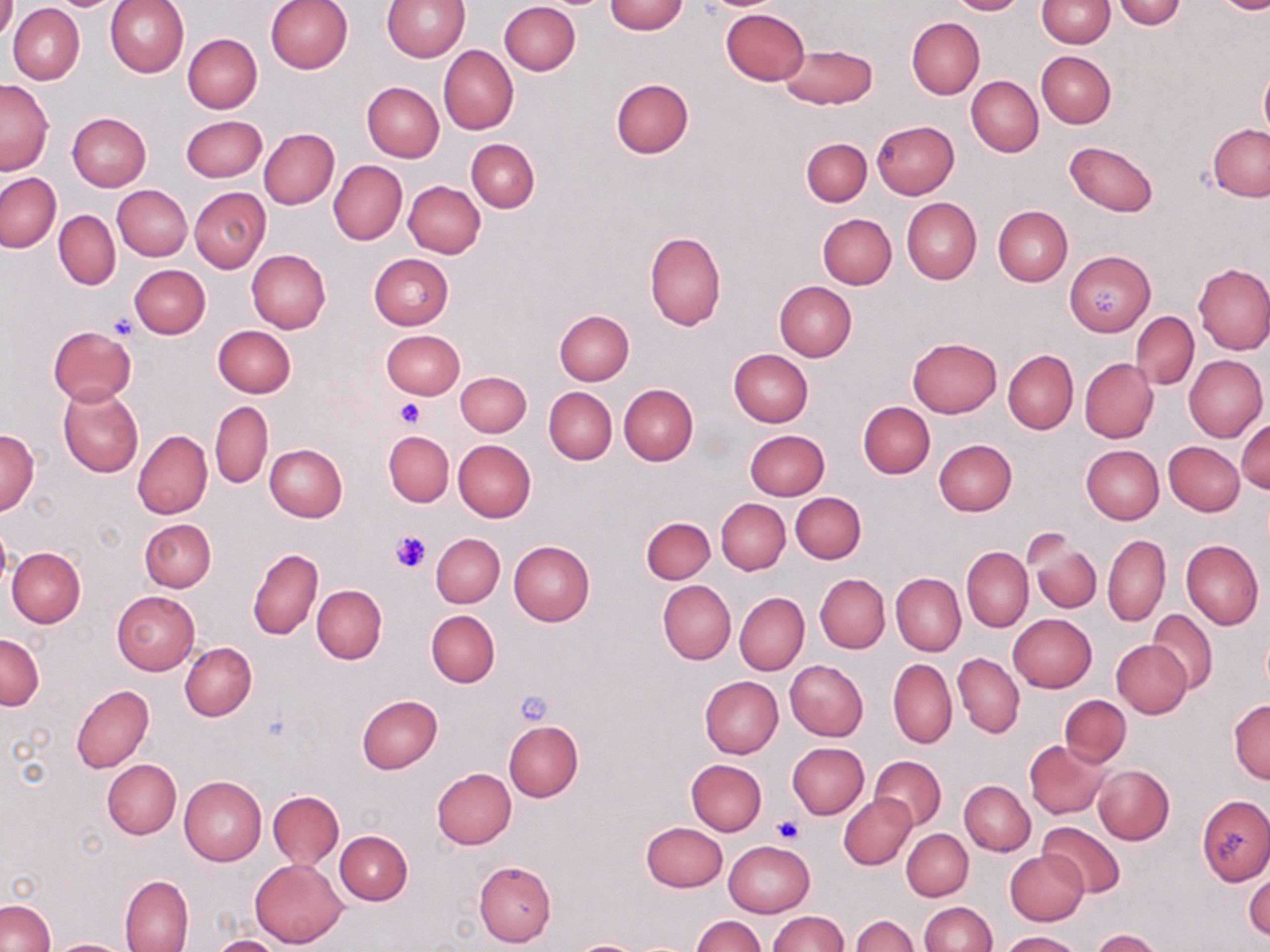

Summary:
  - Coordinate format: approximate bounding boxes as named x1/y1/x2/y2 corners in pixels
  - Platelet locations: (x1=1086, y1=284, x2=1126, y2=320), (x1=108, y1=314, x2=141, y2=340), (x1=395, y1=400, x2=425, y2=427), (x1=389, y1=530, x2=432, y2=574), (x1=514, y1=689, x2=555, y2=728), (x1=774, y1=815, x2=805, y2=843)
  - Uninfected red blood cell locations: (x1=0, y1=0, x2=16, y2=42), (x1=106, y1=0, x2=188, y2=77), (x1=264, y1=0, x2=353, y2=74), (x1=384, y1=0, x2=469, y2=61), (x1=947, y1=0, x2=1028, y2=16), (x1=1037, y1=0, x2=1114, y2=47), (x1=605, y1=1, x2=689, y2=35), (x1=1113, y1=1, x2=1188, y2=27), (x1=1213, y1=1, x2=1270, y2=14), (x1=500, y1=2, x2=581, y2=75), (x1=8, y1=4, x2=84, y2=85), (x1=721, y1=8, x2=808, y2=84), (x1=907, y1=18, x2=985, y2=99), (x1=183, y1=34, x2=261, y2=113), (x1=779, y1=42, x2=876, y2=108), (x1=439, y1=46, x2=518, y2=134), (x1=1036, y1=51, x2=1115, y2=127), (x1=1259, y1=67, x2=1270, y2=141), (x1=967, y1=76, x2=1043, y2=156), (x1=0, y1=79, x2=53, y2=174), (x1=610, y1=79, x2=693, y2=158), (x1=361, y1=82, x2=444, y2=162), (x1=67, y1=113, x2=150, y2=191), (x1=181, y1=115, x2=267, y2=182), (x1=872, y1=121, x2=959, y2=198), (x1=1208, y1=125, x2=1270, y2=200), (x1=259, y1=129, x2=338, y2=210), (x1=801, y1=137, x2=872, y2=207), (x1=466, y1=139, x2=539, y2=213), (x1=1065, y1=142, x2=1158, y2=217), (x1=329, y1=161, x2=407, y2=245), (x1=1, y1=173, x2=61, y2=252), (x1=404, y1=181, x2=485, y2=258), (x1=112, y1=185, x2=192, y2=261), (x1=189, y1=187, x2=270, y2=272), (x1=901, y1=198, x2=980, y2=283), (x1=993, y1=206, x2=1072, y2=286), (x1=53, y1=211, x2=120, y2=290), (x1=817, y1=213, x2=896, y2=289), (x1=645, y1=232, x2=726, y2=330), (x1=247, y1=249, x2=330, y2=333), (x1=1065, y1=250, x2=1155, y2=336), (x1=370, y1=253, x2=453, y2=330), (x1=1193, y1=263, x2=1270, y2=354), (x1=129, y1=264, x2=210, y2=339), (x1=773, y1=281, x2=856, y2=362), (x1=554, y1=310, x2=634, y2=384), (x1=1131, y1=312, x2=1198, y2=390), (x1=213, y1=325, x2=295, y2=397), (x1=48, y1=326, x2=136, y2=405), (x1=381, y1=329, x2=465, y2=399), (x1=908, y1=338, x2=1002, y2=417), (x1=729, y1=348, x2=814, y2=426), (x1=1004, y1=349, x2=1078, y2=434), (x1=739, y1=350, x2=819, y2=498), (x1=1184, y1=354, x2=1267, y2=442), (x1=1080, y1=359, x2=1157, y2=442), (x1=456, y1=371, x2=531, y2=437), (x1=619, y1=383, x2=698, y2=465), (x1=544, y1=386, x2=617, y2=464), (x1=58, y1=387, x2=143, y2=478), (x1=210, y1=401, x2=273, y2=487), (x1=859, y1=402, x2=934, y2=477), (x1=1236, y1=418, x2=1269, y2=493), (x1=0, y1=430, x2=40, y2=515), (x1=744, y1=430, x2=829, y2=500), (x1=133, y1=431, x2=212, y2=519), (x1=383, y1=431, x2=454, y2=507), (x1=453, y1=439, x2=536, y2=521), (x1=933, y1=439, x2=1017, y2=515), (x1=1163, y1=441, x2=1244, y2=516), (x1=264, y1=443, x2=348, y2=522), (x1=1082, y1=445, x2=1164, y2=523), (x1=791, y1=492, x2=866, y2=564), (x1=716, y1=498, x2=789, y2=574), (x1=641, y1=517, x2=715, y2=584), (x1=140, y1=518, x2=216, y2=592), (x1=0, y1=519, x2=11, y2=593), (x1=431, y1=533, x2=504, y2=607), (x1=1103, y1=534, x2=1171, y2=626), (x1=1027, y1=536, x2=1101, y2=612), (x1=1180, y1=539, x2=1264, y2=628), (x1=508, y1=541, x2=594, y2=626), (x1=6, y1=546, x2=86, y2=627), (x1=248, y1=547, x2=322, y2=640), (x1=962, y1=547, x2=1032, y2=632), (x1=816, y1=574, x2=890, y2=653), (x1=891, y1=574, x2=965, y2=655), (x1=657, y1=581, x2=734, y2=665), (x1=312, y1=586, x2=386, y2=663), (x1=112, y1=591, x2=200, y2=674), (x1=735, y1=593, x2=808, y2=674), (x1=1147, y1=609, x2=1218, y2=694), (x1=426, y1=610, x2=500, y2=687), (x1=1008, y1=614, x2=1096, y2=693), (x1=0, y1=633, x2=43, y2=710), (x1=1111, y1=640, x2=1191, y2=717), (x1=179, y1=641, x2=256, y2=721), (x1=953, y1=653, x2=1025, y2=738), (x1=888, y1=657, x2=956, y2=748), (x1=786, y1=660, x2=867, y2=741), (x1=700, y1=676, x2=783, y2=758), (x1=72, y1=685, x2=155, y2=773), (x1=357, y1=695, x2=443, y2=773), (x1=1058, y1=695, x2=1130, y2=767), (x1=1229, y1=699, x2=1270, y2=783), (x1=1043, y1=702, x2=1131, y2=826), (x1=505, y1=720, x2=583, y2=802), (x1=1026, y1=740, x2=1111, y2=818), (x1=788, y1=743, x2=868, y2=818), (x1=870, y1=756, x2=946, y2=830), (x1=103, y1=759, x2=180, y2=839), (x1=686, y1=759, x2=766, y2=836), (x1=1092, y1=764, x2=1174, y2=844), (x1=432, y1=767, x2=516, y2=849), (x1=180, y1=776, x2=266, y2=865), (x1=959, y1=780, x2=1034, y2=855), (x1=268, y1=791, x2=343, y2=870), (x1=839, y1=793, x2=916, y2=869), (x1=1198, y1=796, x2=1270, y2=885), (x1=642, y1=821, x2=727, y2=892), (x1=1038, y1=821, x2=1125, y2=897), (x1=902, y1=829, x2=972, y2=901), (x1=335, y1=830, x2=413, y2=905), (x1=724, y1=841, x2=814, y2=917), (x1=1005, y1=850, x2=1089, y2=925), (x1=249, y1=857, x2=348, y2=947), (x1=474, y1=861, x2=556, y2=948), (x1=1245, y1=861, x2=1270, y2=942), (x1=120, y1=875, x2=193, y2=952), (x1=1, y1=900, x2=55, y2=952), (x1=919, y1=901, x2=997, y2=952), (x1=767, y1=910, x2=847, y2=952), (x1=852, y1=914, x2=917, y2=952), (x1=692, y1=915, x2=765, y2=952), (x1=1092, y1=929, x2=1166, y2=952), (x1=1001, y1=930, x2=1082, y2=952), (x1=209, y1=935, x2=287, y2=952), (x1=48, y1=938, x2=132, y2=951), (x1=570, y1=940, x2=641, y2=952)
  - Slide-level diagnosis: no evidence of blood parasites
  - Stain: May-Grünwald-Giemsa
  - Image size: 1270×952 pixels
  - Field of view: one of a larger specimen
  - Magnification: 1000x
  - Modality: optical microscopy
  - Preparation: thin blood smear